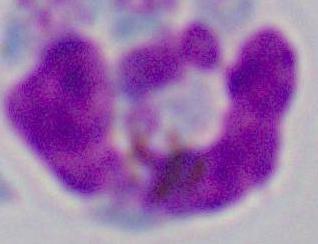
magnification = 1000x
identification = leukocyte
modality = photomicrograph